Report the malaria status of this cell.
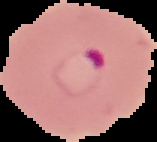

Parasitized.

preparation = thin blood smear
image type = segmented cell region on a black background
image size = 157×142 pixels